Classify this cell by malaria status.
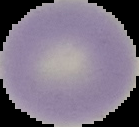

Uninfected.

Summary:
  - Image size: 139×127 pixels
  - Preparation: thin blood film
  - Image type: segmented cell region with the area outside set to black